Outline each blood parasite and name the species.
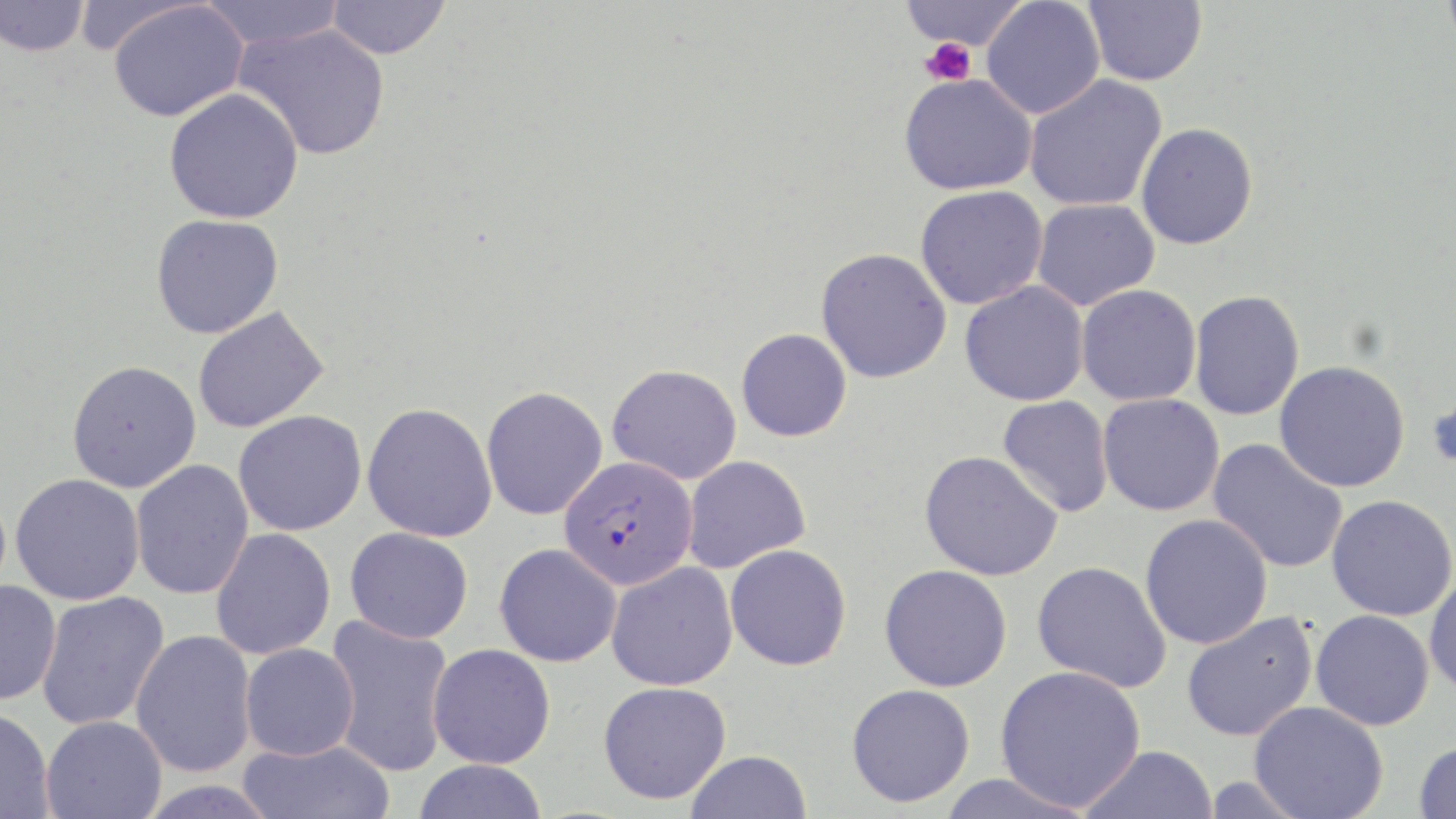

Approximate bounding boxes as [x1, y1, x2, y2] in pixels.
Plasmodium falciparum-infected red blood cells: [559, 456, 698, 590].
No Plasmodium ovale, Plasmodium malariae, Plasmodium vivax, Babesia divergens, or Trypanosoma brucei observed.

Summary:
  - Uninfected red blood cell locations: [0, 0, 90, 57], [197, 0, 347, 51], [325, 0, 451, 60], [898, 0, 1029, 51], [981, 0, 1105, 119], [1083, 0, 1207, 86], [1440, 0, 1456, 55], [108, 2, 248, 122], [234, 23, 390, 160], [899, 73, 1037, 195], [1024, 75, 1167, 212], [164, 88, 304, 224], [1136, 123, 1258, 249], [915, 185, 1047, 310], [1032, 198, 1159, 310], [151, 214, 284, 339], [815, 247, 952, 383], [959, 280, 1089, 406], [1076, 284, 1202, 406], [1189, 290, 1304, 421], [192, 305, 329, 433], [736, 328, 852, 442], [67, 360, 202, 493], [1274, 360, 1410, 492], [607, 363, 742, 484], [1427, 371, 1456, 478], [480, 386, 608, 520], [1097, 393, 1225, 516], [997, 395, 1114, 518], [362, 402, 498, 542], [233, 410, 367, 536], [1208, 438, 1348, 575], [919, 449, 1063, 581], [682, 455, 811, 574], [130, 459, 254, 599], [10, 473, 145, 605], [1326, 494, 1456, 621], [1140, 514, 1273, 649], [345, 527, 473, 643], [210, 528, 336, 660], [494, 543, 622, 667], [725, 544, 852, 671], [1032, 560, 1172, 693], [606, 562, 738, 691], [879, 564, 1011, 692], [1425, 569, 1456, 700], [0, 579, 61, 705], [35, 591, 171, 730], [1310, 609, 1434, 730], [1181, 612, 1319, 741], [324, 615, 455, 777], [130, 630, 257, 778], [240, 643, 359, 761], [427, 643, 556, 768], [995, 665, 1146, 811], [598, 681, 732, 804], [846, 683, 975, 808], [1249, 701, 1388, 819], [0, 708, 55, 819], [41, 715, 167, 819], [238, 738, 396, 819], [1414, 740, 1456, 818], [1079, 744, 1218, 819], [685, 750, 812, 819], [411, 759, 548, 818], [936, 772, 1098, 819], [134, 778, 283, 818]
  - Platelet locations: [922, 38, 975, 86]
  - Slide-level diagnosis: Plasmodium falciparum
  - Magnification: 1000x
  - Preparation: thin blood film
  - Stain: May-Grünwald-Giemsa
  - Field of view: one of a larger specimen
  - Modality: light microscopy
  - Image size: 1456×819 pixels